Name the cell type shown.
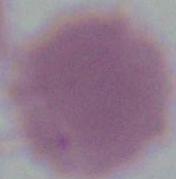
This is an erythrocyte.

Micrograph. 1000x magnification.